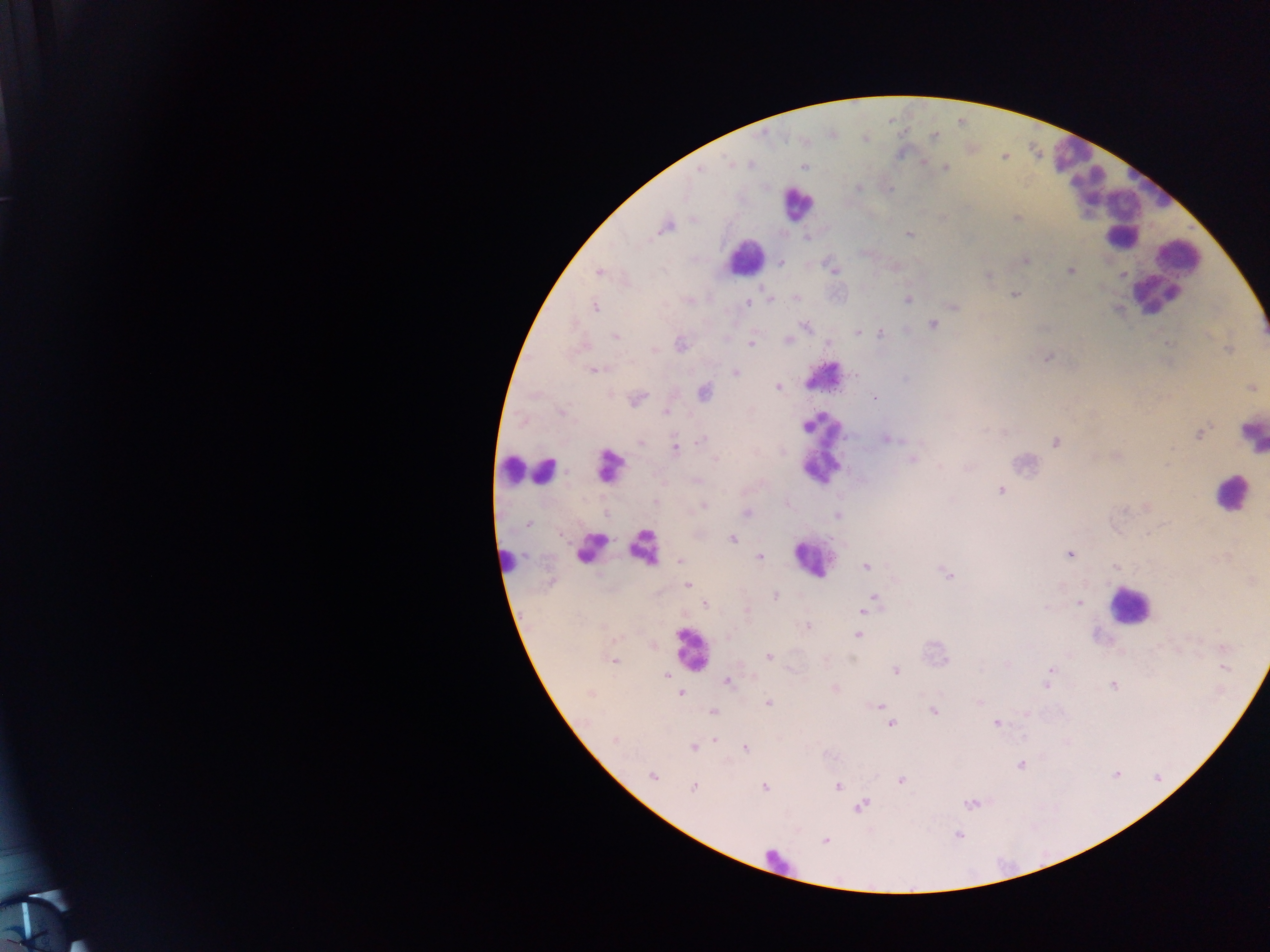
{
  "preparation": "thick blood film",
  "leukocyte_locations": "approximate centers as [x, y] in pixels: [1070, 153], [1088, 186], [1152, 186], [1119, 203], [797, 204], [1127, 241], [745, 257], [1181, 260], [1155, 295], [823, 426], [1251, 434], [610, 466], [818, 466], [513, 469], [543, 470], [1230, 494], [590, 547], [644, 549], [810, 558], [508, 559], [1128, 606], [691, 649], [777, 864]",
  "country": "Ghana",
  "capture": "mobile-phone photograph through a microscope",
  "field_of_view": "single",
  "plasmodium_parasite_locations": "approximate centers as [x, y] in pixels: [935, 136], [750, 163], [732, 164], [804, 166], [945, 168], [699, 169], [858, 188], [1016, 218], [666, 226], [909, 236], [806, 238], [1025, 260], [781, 263], [833, 270], [599, 271], [1070, 271], [988, 276], [1014, 294], [772, 299], [795, 299], [688, 300], [908, 300], [748, 303], [955, 306], [594, 307], [933, 325], [804, 326], [858, 332], [881, 333], [616, 336], [788, 340], [751, 342], [680, 344], [828, 344], [654, 349], [1227, 350], [1048, 358], [594, 370], [736, 373], [855, 374], [778, 387], [1251, 388], [704, 392], [875, 397], [637, 399], [667, 412], [562, 413], [1199, 434], [703, 439], [887, 439], [640, 443], [1056, 443], [675, 448], [1171, 449], [1116, 457], [716, 460], [912, 460], [941, 466], [696, 480], [1001, 491], [655, 501], [703, 506], [747, 513], [837, 516], [528, 523], [732, 539], [1069, 554], [760, 557], [680, 560], [866, 566], [947, 573], [687, 585], [775, 596], [874, 598], [1079, 603], [705, 604], [1046, 608], [747, 611], [863, 611], [807, 626], [858, 635], [727, 637], [1224, 648], [769, 657], [613, 661], [1224, 668], [895, 670], [1050, 670], [666, 675], [1048, 677], [728, 682], [1046, 685], [1113, 685], [835, 688], [680, 693], [590, 694], [979, 701], [767, 703], [879, 705], [933, 711], [713, 712], [1026, 714], [891, 723], [996, 723], [716, 738], [615, 739], [692, 747], [745, 748], [1020, 765], [652, 776], [901, 780], [837, 786], [693, 787], [765, 787], [969, 803], [861, 806], [956, 835], [825, 841]",
  "image_size": "1270×952 pixels"
}